Report the malaria status of this cell.
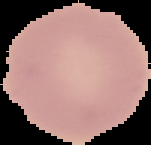

It is uninfected.

Summary:
  - Image size: 151×145 pixels
  - Preparation: thin blood film
  - Image type: segmented cell region on a black background